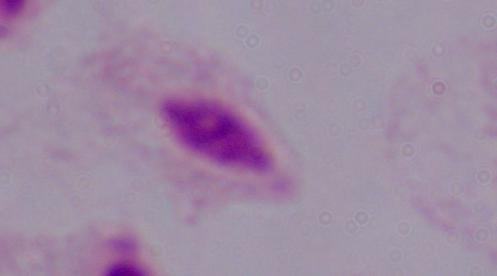

magnification: 1000x
modality: photomicrograph
identification: trichomonad